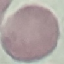
result: no malaria parasites seen
image_type: automatically extracted cell patch, resized to 64 × 64 pixels
stain: Giemsa
preparation: thin smear
capture: smartphone through the microscope eyepiece